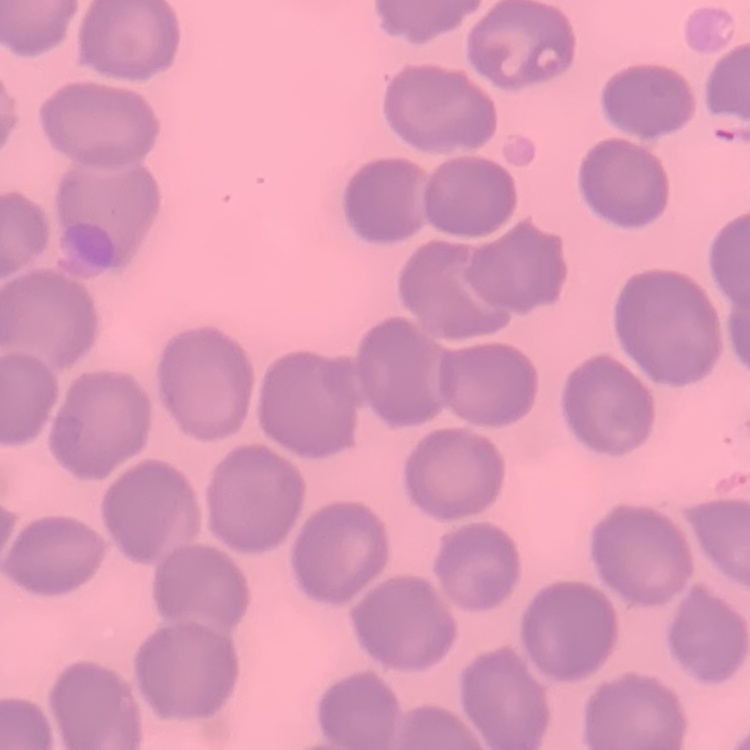

Summary:
  - Red blood cell morphology: no rouleaux formation
  - Stain: Field's or Giemsa
  - Image type: square crop of a larger photomicrograph
  - Preparation: thin blood film